Give the position of every Plasmodium parasite visible.
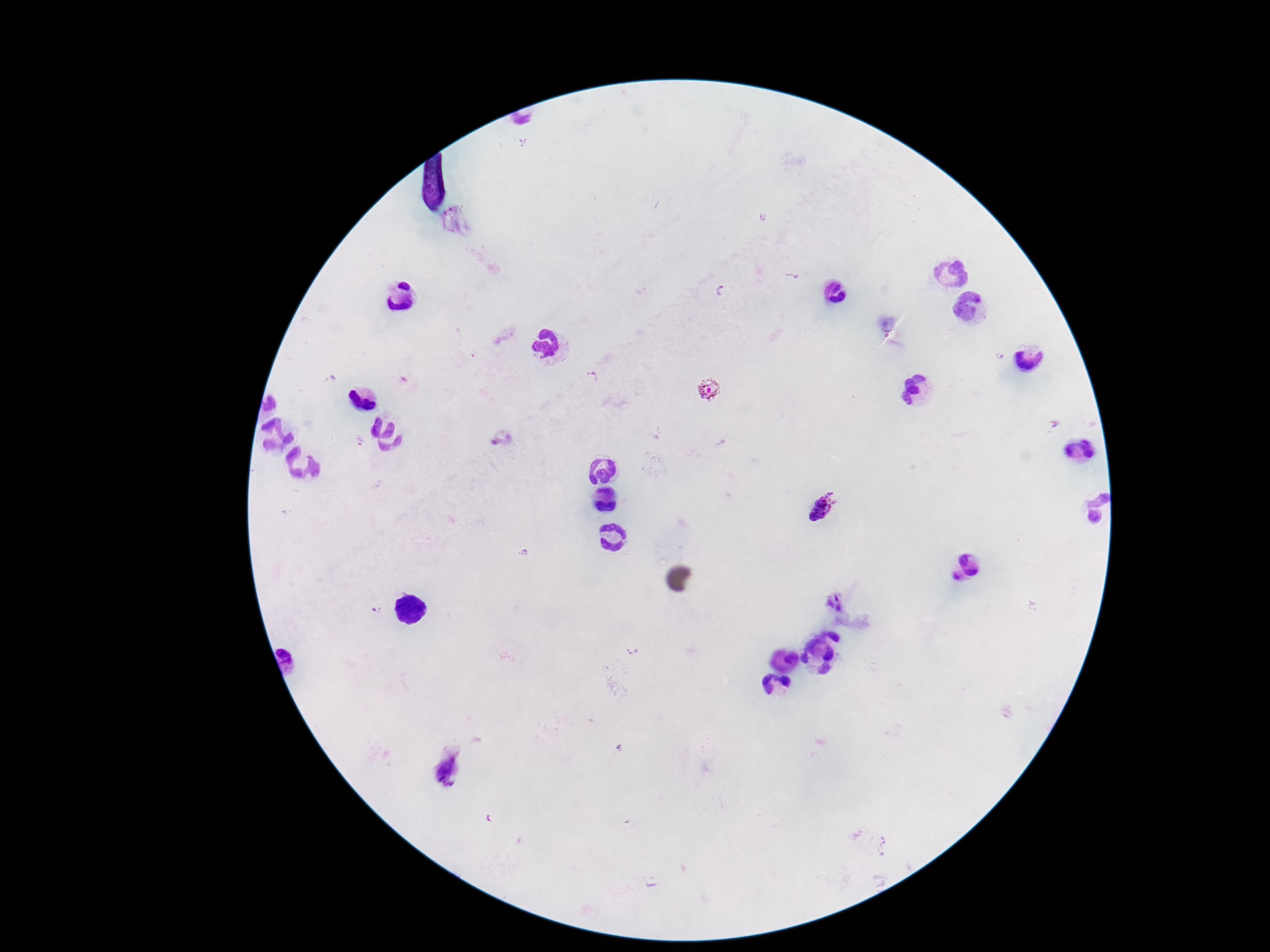

Approximate centers as [x, y] in pixels.
Plasmodium parasites: [593, 375], [707, 391], [359, 442], [824, 505].

Patient malaria status: positive. Photographed through the microscope eyepiece with a smartphone camera. Giemsa stain. 100x magnification. Image is 1270×952 pixels. Thick peripheral-blood smear. One field from this slide.